Name the cell type shown.
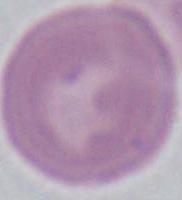
This is an erythrocyte.

Micrograph. 1000x magnification.